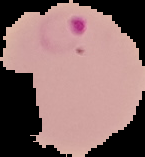

From a thin blood smear. The area outside the segmented cell region is set to black. Image is 145×157 pixels. Malaria status: parasitized.